Identify the parasite.
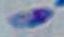
This is Toxoplasma gondii.

Summary:
  - Magnification: 1000x
  - Modality: photomicrograph